Identify the parasite.
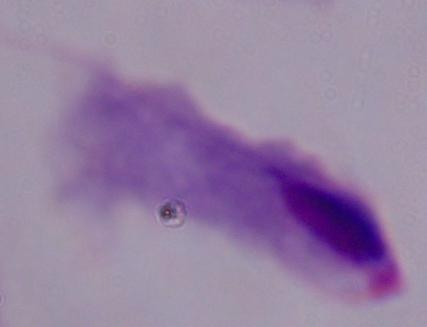

A trichomonad.

magnification = 1000x
modality = photomicrograph